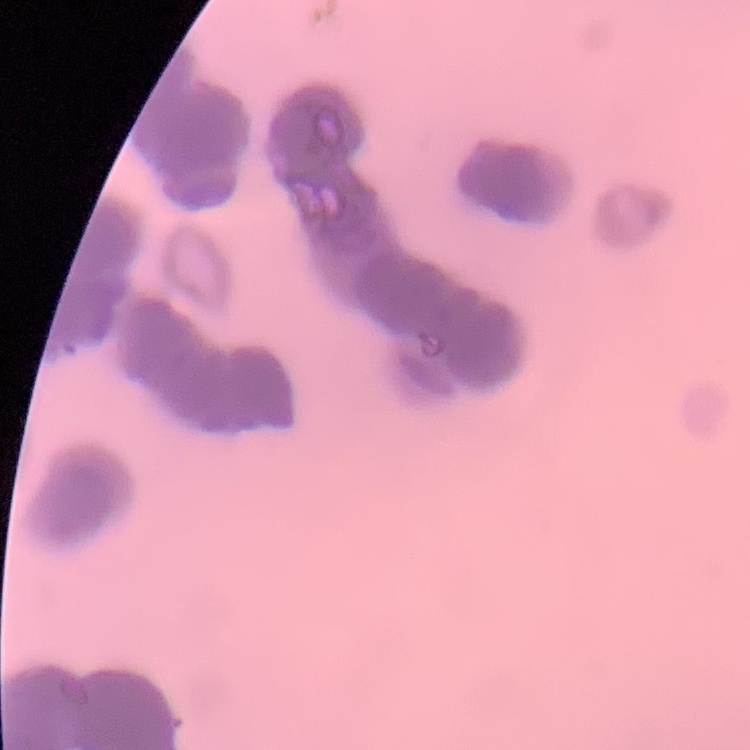 The red blood cells exhibit rouleaux formation. Thin blood film. Field's or Giemsa stain. Square crop of a larger photomicrograph.